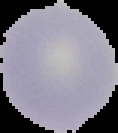

image_size: 118×133 pixels
image_type: segmented cell region with the area outside set to black
malaria_status: uninfected
preparation: thin blood film